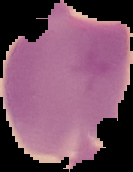

preparation: thin blood smear
image_size: 133×172 pixels
image_type: cell region segmented out of the field of view; surrounding area masked to black
malaria_status: uninfected